Identify the parasite.
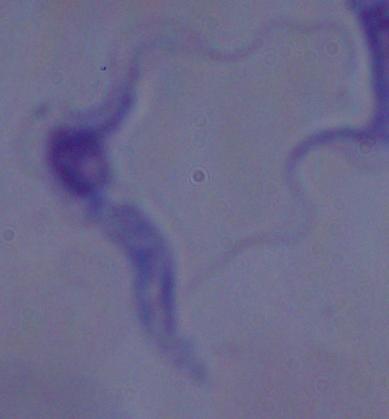
This is a trypanosome.

Captured at 1000x magnification. Photomicrograph.